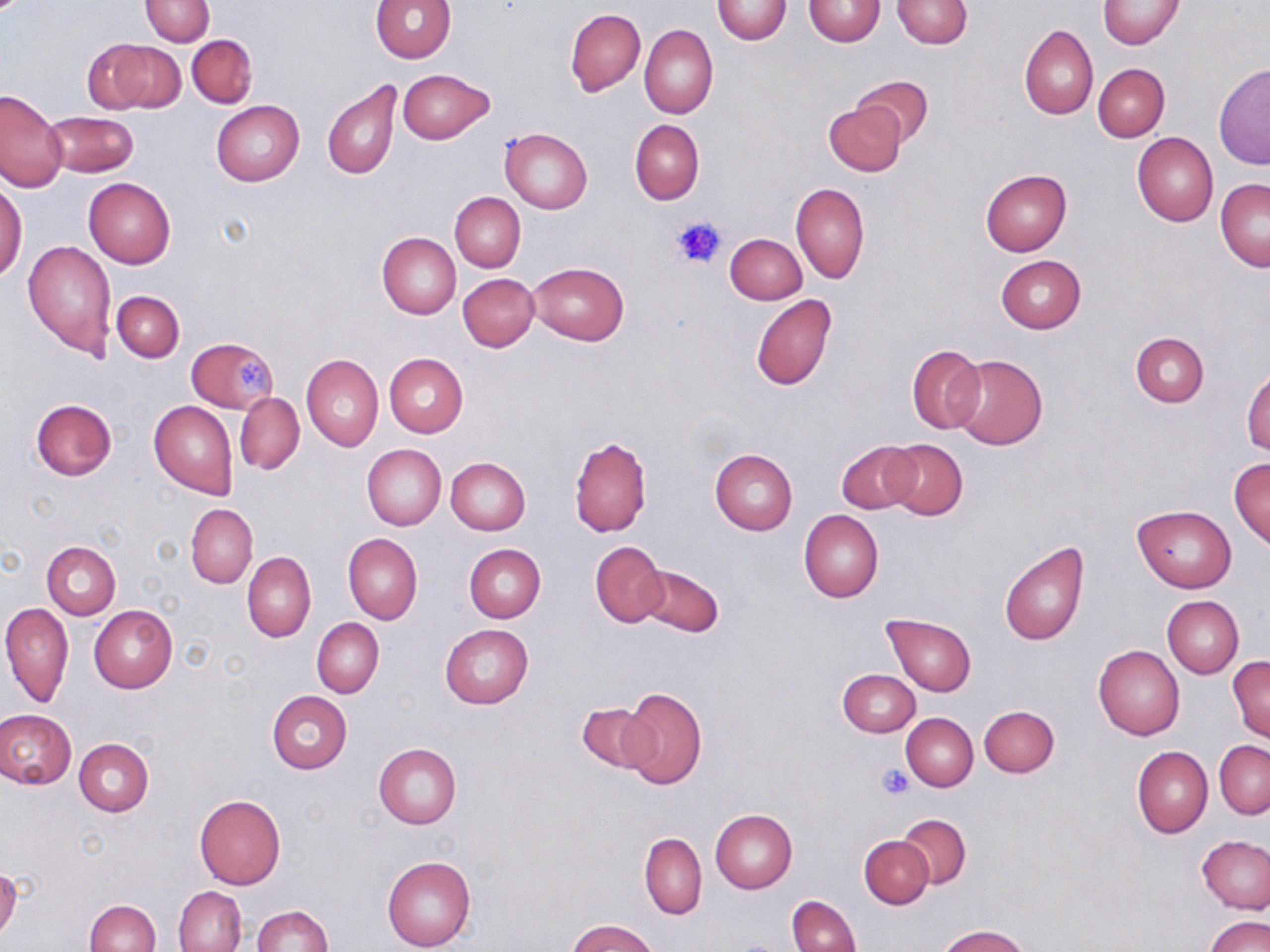

{
  "slide_level_diagnosis": "negative for blood parasites",
  "platelet_locations": "approximate bounding boxes as (x1,y1)-(x2,y2) corner pairs in pixels: (672,216)-(725,269), (235,358)-(273,398), (876,764)-(914,799)",
  "image_size": "1270×952 pixels",
  "uninfected_red_blood_cell_locations": "approximate bounding boxes as (x1,y1)-(x2,y2) corner pairs in pixels: (139,0)-(214,45), (370,0)-(457,62), (711,0)-(792,44), (803,0)-(886,45), (892,0)-(972,49), (1097,0)-(1183,49), (566,8)-(645,96), (639,23)-(717,118), (1019,24)-(1098,120), (187,34)-(257,108), (100,40)-(187,112), (1093,63)-(1170,141), (1213,65)-(1270,170), (398,68)-(492,144), (853,75)-(932,145), (322,79)-(401,179), (0,89)-(66,192), (211,100)-(304,186), (823,102)-(907,176), (43,110)-(139,178), (631,119)-(704,205), (500,127)-(593,213), (1132,132)-(1218,226), (980,169)-(1072,256), (83,177)-(175,270), (1215,177)-(1269,272), (791,182)-(869,285), (0,183)-(27,283), (449,192)-(525,272), (377,232)-(460,318), (725,233)-(806,304), (23,239)-(116,359), (995,254)-(1087,334), (529,262)-(629,345), (458,273)-(539,351), (111,290)-(185,362), (751,295)-(836,392), (1130,333)-(1209,407), (187,335)-(279,413), (907,343)-(986,435), (384,353)-(468,437), (301,354)-(383,451), (949,354)-(1048,449), (1243,367)-(1270,454), (235,393)-(305,474), (31,399)-(117,480), (149,400)-(237,498), (569,437)-(652,536), (881,438)-(968,520), (835,439)-(920,514), (361,444)-(446,530), (710,448)-(797,536), (1229,457)-(1270,549), (446,458)-(530,535), (186,503)-(258,588), (1131,504)-(1237,592), (799,509)-(884,602), (344,533)-(422,624), (1000,539)-(1089,646), (591,541)-(668,628), (42,542)-(120,619), (464,544)-(545,623), (242,552)-(316,643), (634,564)-(724,637), (1162,596)-(1243,679), (1,601)-(72,709), (88,605)-(177,693), (882,613)-(976,696), (312,618)-(384,698), (439,624)-(534,708), (1093,646)-(1184,740), (1227,656)-(1270,742), (838,669)-(919,736), (619,685)-(709,789), (266,691)-(352,774), (575,701)-(658,774), (979,705)-(1059,777), (0,709)-(77,790), (902,713)-(978,791), (75,738)-(154,817), (1215,740)-(1269,819), (373,743)-(462,829), (1132,746)-(1212,837), (195,794)-(285,889), (710,809)-(798,893), (895,813)-(971,889), (640,832)-(706,920), (860,835)-(933,909), (1198,836)-(1270,914), (382,855)-(476,951), (0,863)-(21,940), (174,887)-(247,952), (786,894)-(860,952), (85,898)-(159,952), (250,905)-(333,951), (1205,915)-(1269,952), (567,919)-(659,952), (938,924)-(1028,952)",
  "field_of_view": "single",
  "magnification": "1000x",
  "stain": "May-Grünwald-Giemsa",
  "modality": "optical microscopy",
  "preparation": "thin blood film"
}